Outline each Plasmodium ovale-infected red blood cell.
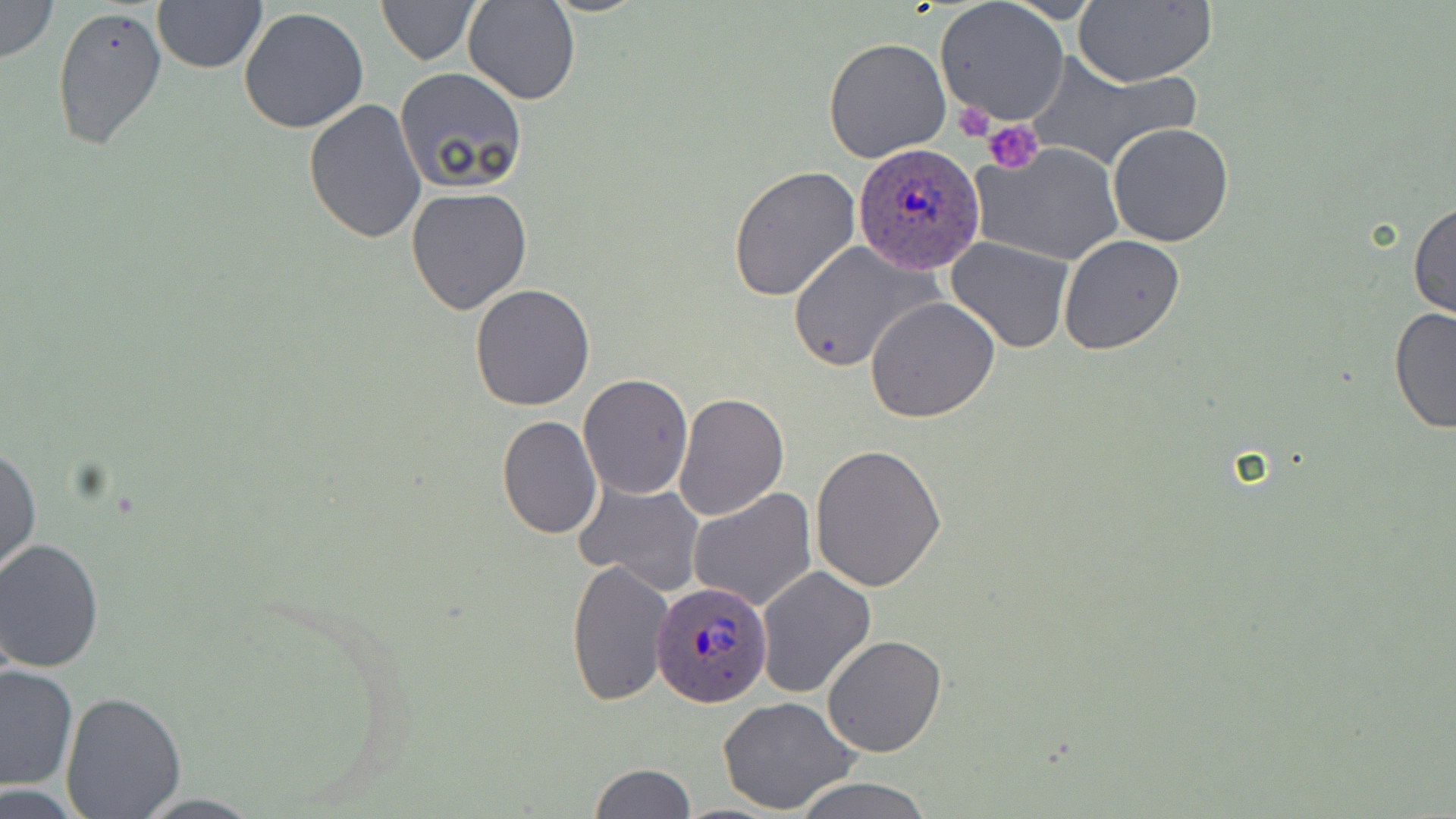

Approximate bounding boxes as [x1, y1, x2, y2] in pixels.
Plasmodium ovale-infected red blood cells: [855, 142, 985, 274], [655, 579, 772, 706].

Uninfected red blood cell locations: [1, 0, 60, 63], [152, 0, 267, 74], [463, 0, 579, 104], [378, 1, 481, 65], [936, 1, 1069, 126], [1073, 2, 1215, 86], [51, 4, 169, 152], [238, 7, 370, 135], [823, 37, 951, 164], [1025, 49, 1202, 172], [395, 67, 526, 193], [303, 98, 428, 245], [1107, 122, 1235, 248], [973, 142, 1124, 267], [727, 165, 862, 305], [405, 186, 534, 317], [1409, 198, 1455, 323], [1058, 235, 1185, 356], [947, 237, 1075, 352], [788, 241, 938, 372], [469, 283, 597, 411], [864, 296, 999, 423], [1389, 304, 1456, 436], [579, 374, 693, 499], [675, 390, 789, 523], [493, 396, 688, 522], [497, 414, 603, 540], [1, 439, 40, 580], [810, 442, 947, 591], [577, 480, 705, 595], [687, 487, 817, 612], [0, 539, 105, 672], [565, 556, 675, 709], [756, 566, 875, 697], [821, 633, 947, 757], [0, 664, 78, 793], [59, 690, 185, 815], [716, 696, 860, 815], [587, 763, 695, 818], [789, 776, 933, 819]. Platelet locations: [956, 102, 998, 143], [984, 119, 1043, 173]. Slide-level diagnosis: Plasmodium ovale. 1000x magnification. Thin blood film. May-Grünwald-Giemsa-stained preparation. Single field of view. Image is 1456×819 pixels. Optical microscopy.